Locate and identify every blood parasite.
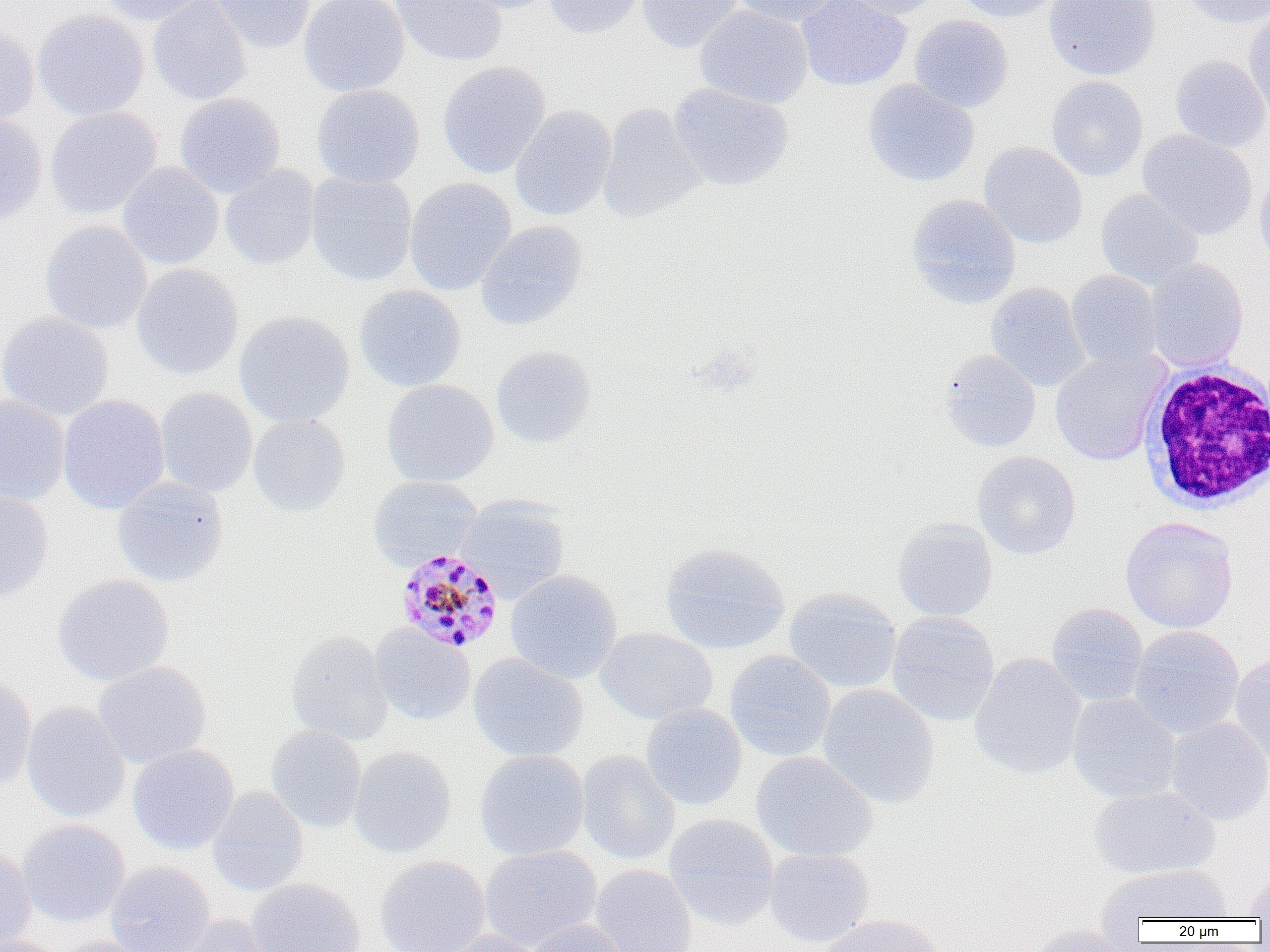
Approximate bounding boxes as named x1/y1/x2/y2 corners in pixels.
Plasmodium malariae-infected red blood cells: (x1=395, y1=548, x2=504, y2=653).
No Plasmodium falciparum, Plasmodium ovale, Plasmodium vivax, Babesia divergens, or Trypanosoma brucei observed.

slide-level diagnosis = Plasmodium malariae
preparation = thin blood film
modality = light microscopy
white blood cell locations = approximate bounding boxes as named x1/y1/x2/y2 corners in pixels: (x1=1139, y1=363, x2=1269, y2=512)
magnification = 1000x
image size = 1270×952 pixels
field of view = one of a larger specimen
uninfected red blood cell locations = approximate bounding boxes as named x1/y1/x2/y2 corners in pixels: (x1=97, y1=0, x2=210, y2=25), (x1=147, y1=0, x2=252, y2=105), (x1=211, y1=0, x2=316, y2=52), (x1=298, y1=0, x2=409, y2=96), (x1=392, y1=0, x2=507, y2=66), (x1=447, y1=0, x2=559, y2=14), (x1=543, y1=0, x2=646, y2=38), (x1=637, y1=0, x2=743, y2=53), (x1=727, y1=0, x2=843, y2=27), (x1=796, y1=0, x2=912, y2=92), (x1=844, y1=0, x2=943, y2=19), (x1=955, y1=0, x2=1066, y2=22), (x1=1043, y1=0, x2=1161, y2=81), (x1=1179, y1=0, x2=1270, y2=29), (x1=695, y1=5, x2=814, y2=108), (x1=32, y1=9, x2=149, y2=120), (x1=1243, y1=10, x2=1270, y2=119), (x1=909, y1=14, x2=1013, y2=113), (x1=0, y1=21, x2=39, y2=125), (x1=1169, y1=55, x2=1270, y2=152), (x1=437, y1=61, x2=551, y2=179), (x1=1046, y1=75, x2=1148, y2=181), (x1=862, y1=79, x2=980, y2=187), (x1=669, y1=83, x2=794, y2=191), (x1=311, y1=84, x2=425, y2=189), (x1=175, y1=92, x2=285, y2=197), (x1=598, y1=103, x2=705, y2=224), (x1=510, y1=105, x2=616, y2=221), (x1=45, y1=106, x2=161, y2=218), (x1=0, y1=112, x2=47, y2=224), (x1=1137, y1=130, x2=1257, y2=240), (x1=978, y1=141, x2=1088, y2=248), (x1=117, y1=162, x2=224, y2=270), (x1=220, y1=165, x2=319, y2=270), (x1=1254, y1=166, x2=1270, y2=275), (x1=306, y1=172, x2=417, y2=285), (x1=405, y1=177, x2=517, y2=296), (x1=1095, y1=188, x2=1203, y2=291), (x1=906, y1=194, x2=1022, y2=309), (x1=476, y1=220, x2=587, y2=331), (x1=40, y1=221, x2=152, y2=335), (x1=1145, y1=258, x2=1248, y2=372), (x1=131, y1=264, x2=244, y2=380), (x1=1066, y1=270, x2=1162, y2=371), (x1=986, y1=282, x2=1090, y2=391), (x1=354, y1=285, x2=466, y2=392), (x1=0, y1=311, x2=113, y2=421), (x1=234, y1=311, x2=355, y2=427), (x1=491, y1=345, x2=597, y2=448), (x1=1049, y1=348, x2=1170, y2=467), (x1=939, y1=349, x2=1041, y2=453), (x1=381, y1=379, x2=498, y2=487), (x1=155, y1=388, x2=258, y2=497), (x1=0, y1=393, x2=70, y2=505), (x1=58, y1=394, x2=169, y2=514), (x1=248, y1=413, x2=350, y2=517), (x1=972, y1=451, x2=1081, y2=559), (x1=367, y1=475, x2=482, y2=570), (x1=112, y1=477, x2=230, y2=587), (x1=0, y1=487, x2=54, y2=602), (x1=456, y1=496, x2=571, y2=602), (x1=1120, y1=516, x2=1239, y2=633), (x1=892, y1=518, x2=998, y2=622), (x1=659, y1=542, x2=790, y2=655), (x1=505, y1=570, x2=622, y2=684), (x1=52, y1=574, x2=174, y2=685), (x1=784, y1=587, x2=903, y2=694), (x1=1046, y1=601, x2=1149, y2=707), (x1=885, y1=611, x2=1000, y2=727), (x1=370, y1=624, x2=476, y2=725), (x1=1128, y1=625, x2=1245, y2=739), (x1=595, y1=627, x2=717, y2=724), (x1=285, y1=630, x2=393, y2=746), (x1=724, y1=650, x2=836, y2=762), (x1=468, y1=653, x2=588, y2=762), (x1=970, y1=653, x2=1087, y2=780), (x1=1229, y1=654, x2=1270, y2=764), (x1=92, y1=660, x2=211, y2=768), (x1=0, y1=671, x2=37, y2=790), (x1=817, y1=683, x2=940, y2=809), (x1=1067, y1=692, x2=1182, y2=804), (x1=21, y1=701, x2=130, y2=823), (x1=641, y1=704, x2=747, y2=810), (x1=1166, y1=716, x2=1270, y2=825), (x1=266, y1=724, x2=367, y2=833), (x1=128, y1=743, x2=239, y2=854), (x1=349, y1=746, x2=457, y2=858), (x1=475, y1=749, x2=589, y2=861), (x1=576, y1=750, x2=680, y2=865), (x1=751, y1=752, x2=877, y2=863), (x1=1088, y1=785, x2=1220, y2=880), (x1=207, y1=786, x2=309, y2=897), (x1=664, y1=814, x2=780, y2=930), (x1=17, y1=819, x2=130, y2=928), (x1=0, y1=844, x2=35, y2=951), (x1=478, y1=846, x2=602, y2=951), (x1=764, y1=847, x2=874, y2=948), (x1=375, y1=855, x2=490, y2=952), (x1=105, y1=861, x2=215, y2=952), (x1=1095, y1=863, x2=1233, y2=927), (x1=590, y1=864, x2=698, y2=952), (x1=1242, y1=870, x2=1270, y2=920), (x1=247, y1=877, x2=366, y2=952), (x1=816, y1=913, x2=947, y2=952), (x1=176, y1=914, x2=280, y2=952), (x1=524, y1=919, x2=630, y2=952), (x1=1026, y1=923, x2=1134, y2=952), (x1=442, y1=930, x2=548, y2=952), (x1=1, y1=935, x2=71, y2=952), (x1=52, y1=935, x2=155, y2=952)